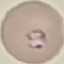

Summary:
  - Malaria status: parasitized
  - Preparation: thin blood film
  - Image type: cell patch, automatically extracted from a larger field of view and resized to 64 × 64 pixels
  - Stain: Giemsa
  - Capture: smartphone through the microscope eyepiece